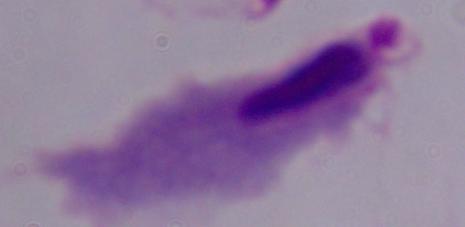
Summary:
  - Magnification: 1000x
  - Modality: photomicrograph
  - Identification: trichomonad